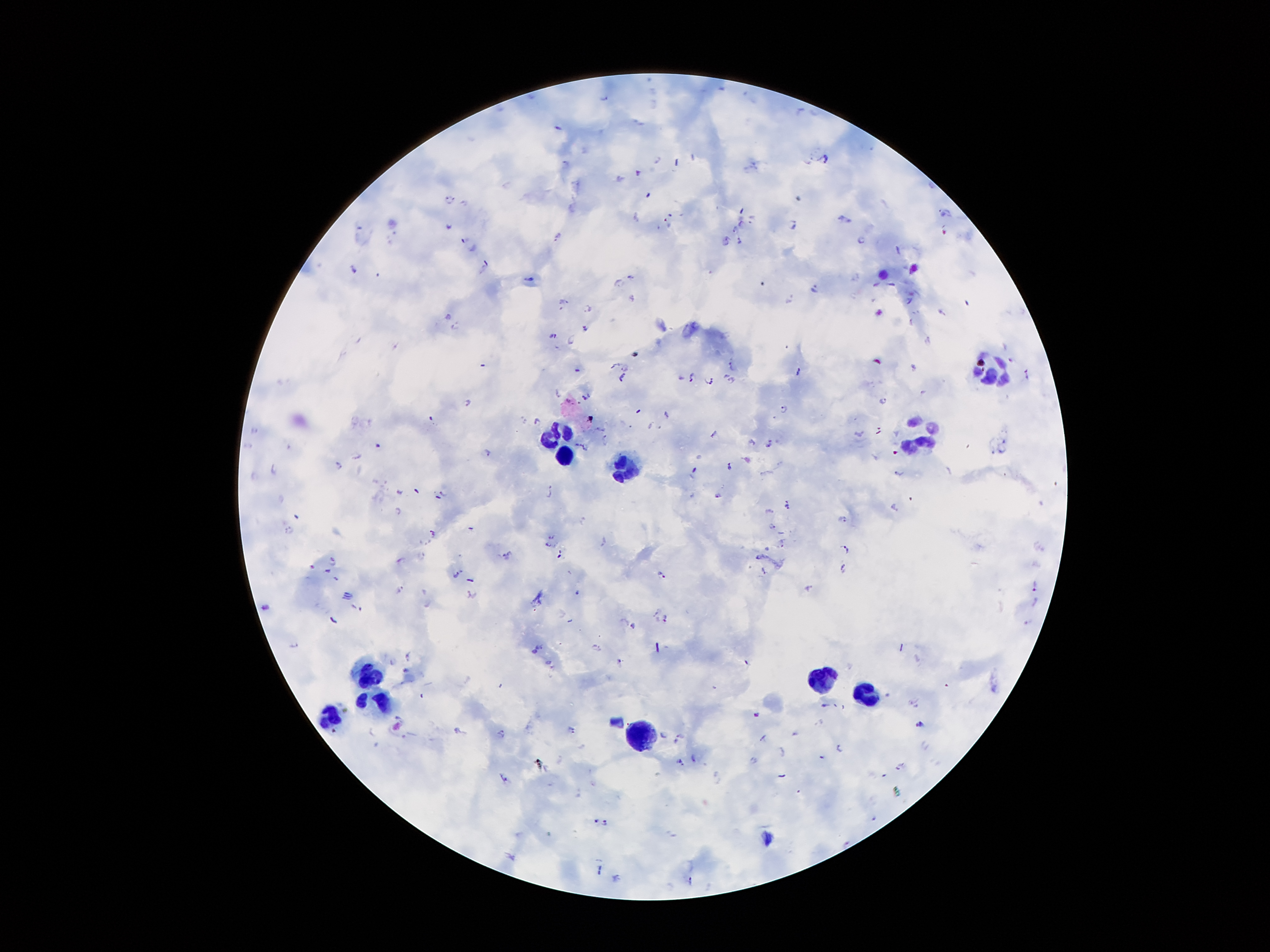

Approximate centers as (x, y) in pixels.
Summary:
  - Plasmodium parasite locations: (604, 98), (656, 158), (825, 160), (639, 173), (647, 195), (451, 198), (946, 212), (636, 215), (845, 218), (753, 219), (667, 222), (793, 223), (448, 224), (742, 224), (734, 230), (557, 236), (725, 239), (465, 240), (739, 241), (861, 241), (484, 264), (353, 269), (632, 277), (857, 279), (531, 280), (620, 283), (876, 283), (892, 284), (812, 287), (632, 297), (790, 299), (907, 300), (560, 301), (587, 309), (942, 311), (454, 326), (584, 327), (552, 335), (573, 340), (928, 340), (734, 365), (624, 366), (913, 367), (576, 370), (799, 370), (692, 375), (725, 375), (680, 376), (622, 379), (707, 380), (730, 380), (559, 394), (586, 396), (568, 400), (883, 400), (467, 402), (783, 407), (638, 410), (667, 414), (538, 421), (658, 426), (254, 429), (601, 429), (714, 433), (859, 434), (577, 444), (753, 444), (769, 445), (585, 446), (1001, 448), (992, 450), (894, 452), (488, 453), (358, 456), (699, 456), (337, 464), (729, 465), (275, 470), (695, 470), (899, 473), (416, 491), (398, 492), (444, 494), (548, 494), (716, 494), (787, 504), (894, 508), (397, 510), (842, 518), (773, 526), (471, 529), (291, 530), (432, 535), (552, 537), (604, 542), (781, 542), (547, 545), (846, 547), (507, 556), (331, 560), (400, 560), (313, 566), (843, 566), (328, 570), (455, 574), (662, 575), (336, 578), (469, 580), (1034, 584), (810, 586), (399, 588), (579, 592), (470, 594), (1035, 601), (264, 607), (356, 607), (656, 611), (665, 618), (633, 624), (294, 643), (542, 646), (536, 647), (597, 647), (534, 652), (407, 656), (619, 661), (391, 662), (550, 662), (406, 669), (500, 685), (823, 704), (755, 714), (919, 722), (458, 729), (572, 729), (501, 732), (664, 734), (681, 734), (839, 748), (823, 757), (752, 758), (681, 761), (897, 765), (504, 778), (595, 819), (604, 823), (845, 841), (616, 877), (689, 880)
  - Leukocyte locations: (996, 367), (557, 436), (927, 437), (562, 455), (624, 468), (369, 670), (821, 681), (865, 687), (380, 700), (332, 716), (637, 731)
  - Stain: Giemsa
  - Patient malaria status: infected with Plasmodium falciparum
  - Field of view: one from this slide
  - Capture: smartphone camera through the microscope eyepiece
  - Preparation: thick peripheral-blood smear
  - Image size: 1270×952 pixels
  - Magnification: 100x